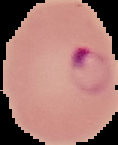
{
  "preparation": "thin blood smear",
  "malaria_status": "parasitized",
  "image_size": "118×145 pixels",
  "image_type": "cell region segmented out of the field of view; surrounding area masked to black"
}